Name the parasite shown.
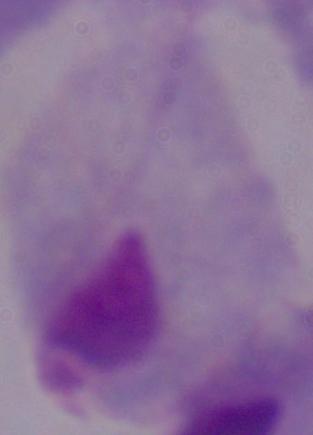
This is a trichomonad.

Summary:
  - Magnification: 1000x
  - Modality: photomicrograph